Assess this cell for malaria.
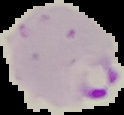

It is parasitized.

Summary:
  - Preparation: thin blood smear
  - Image type: segmented cell region on a black background
  - Image size: 124×115 pixels